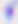
Summary:
  - Magnification: 400x
  - Modality: micrograph
  - Identification: Toxoplasma gondii